Outline each Plasmodium falciparum-infected red blood cell.
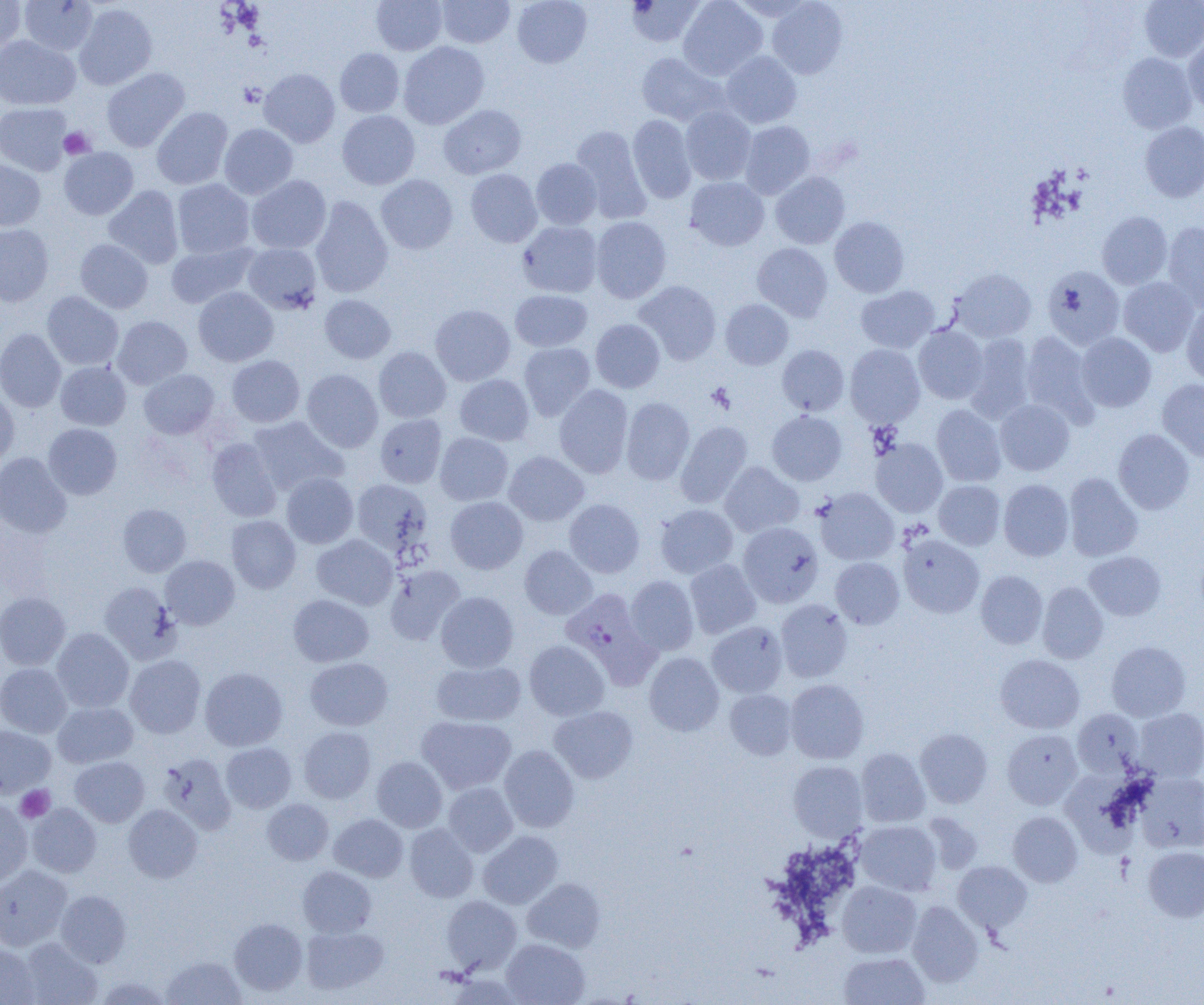

Approximate bounding boxes as named x1/y1/x2/y2 corners in pixels.
Plasmodium falciparum-infected red blood cells: (x1=560, y1=588, x2=657, y2=685).

slide_level_diagnosis: Plasmodium falciparum
field_of_view: single
uninfected_red_blood_cell_locations: 'approximate bounding boxes as named x1/y1/x2/y2 corners in pixels: (x1=0, y1=0, x2=26, y2=55), (x1=19, y1=0, x2=98, y2=56), (x1=371, y1=0, x2=447, y2=55), (x1=436, y1=0, x2=514, y2=48), (x1=512, y1=0, x2=592, y2=68), (x1=626, y1=0, x2=706, y2=47), (x1=678, y1=0, x2=768, y2=80), (x1=1139, y1=0, x2=1204, y2=62), (x1=767, y1=1, x2=848, y2=78), (x1=74, y1=4, x2=158, y2=90), (x1=0, y1=36, x2=80, y2=110), (x1=1183, y1=36, x2=1204, y2=113), (x1=398, y1=42, x2=489, y2=129), (x1=335, y1=48, x2=404, y2=117), (x1=720, y1=51, x2=801, y2=128), (x1=636, y1=52, x2=725, y2=125), (x1=1118, y1=53, x2=1197, y2=134), (x1=101, y1=68, x2=190, y2=152), (x1=259, y1=68, x2=340, y2=148), (x1=0, y1=103, x2=72, y2=175), (x1=439, y1=105, x2=525, y2=179), (x1=151, y1=107, x2=233, y2=190), (x1=680, y1=107, x2=756, y2=185), (x1=337, y1=110, x2=420, y2=189), (x1=628, y1=114, x2=697, y2=204), (x1=739, y1=121, x2=815, y2=199), (x1=1139, y1=121, x2=1204, y2=202), (x1=219, y1=123, x2=298, y2=199), (x1=570, y1=126, x2=651, y2=223), (x1=59, y1=147, x2=139, y2=219), (x1=531, y1=158, x2=602, y2=229), (x1=0, y1=159, x2=45, y2=230), (x1=465, y1=169, x2=542, y2=248), (x1=770, y1=171, x2=850, y2=249), (x1=376, y1=174, x2=457, y2=254), (x1=246, y1=175, x2=331, y2=254), (x1=685, y1=177, x2=769, y2=250), (x1=172, y1=179, x2=255, y2=259), (x1=103, y1=185, x2=184, y2=269), (x1=310, y1=196, x2=393, y2=298), (x1=1097, y1=211, x2=1172, y2=289), (x1=591, y1=216, x2=671, y2=303), (x1=830, y1=216, x2=909, y2=297), (x1=517, y1=221, x2=603, y2=297), (x1=1162, y1=222, x2=1204, y2=311), (x1=0, y1=224, x2=54, y2=306), (x1=75, y1=239, x2=153, y2=313), (x1=166, y1=241, x2=258, y2=309), (x1=243, y1=243, x2=322, y2=314), (x1=752, y1=243, x2=833, y2=321), (x1=1042, y1=266, x2=1125, y2=349), (x1=951, y1=269, x2=1036, y2=342), (x1=1118, y1=277, x2=1199, y2=356), (x1=634, y1=281, x2=721, y2=365), (x1=193, y1=286, x2=279, y2=366), (x1=855, y1=286, x2=940, y2=353), (x1=510, y1=289, x2=593, y2=352), (x1=42, y1=291, x2=124, y2=370), (x1=319, y1=294, x2=396, y2=364), (x1=720, y1=299, x2=793, y2=369), (x1=1181, y1=303, x2=1204, y2=386), (x1=430, y1=304, x2=515, y2=385), (x1=112, y1=316, x2=192, y2=389), (x1=591, y1=318, x2=665, y2=393), (x1=914, y1=325, x2=989, y2=404), (x1=0, y1=328, x2=66, y2=412), (x1=1021, y1=330, x2=1100, y2=426), (x1=1076, y1=333, x2=1156, y2=412), (x1=964, y1=334, x2=1035, y2=422), (x1=519, y1=343, x2=595, y2=421), (x1=845, y1=344, x2=925, y2=427), (x1=777, y1=345, x2=849, y2=416), (x1=374, y1=346, x2=451, y2=423), (x1=227, y1=355, x2=305, y2=427), (x1=55, y1=361, x2=131, y2=430), (x1=139, y1=369, x2=219, y2=439), (x1=302, y1=369, x2=383, y2=452), (x1=454, y1=374, x2=535, y2=445), (x1=1157, y1=379, x2=1204, y2=462), (x1=554, y1=384, x2=633, y2=478), (x1=0, y1=389, x2=19, y2=467), (x1=621, y1=397, x2=695, y2=485), (x1=995, y1=399, x2=1074, y2=475), (x1=931, y1=404, x2=1006, y2=486), (x1=767, y1=410, x2=847, y2=485), (x1=375, y1=414, x2=447, y2=488), (x1=248, y1=416, x2=349, y2=496), (x1=676, y1=421, x2=752, y2=508), (x1=43, y1=424, x2=122, y2=499), (x1=1113, y1=428, x2=1195, y2=514), (x1=435, y1=432, x2=513, y2=506), (x1=207, y1=437, x2=283, y2=522), (x1=871, y1=438, x2=948, y2=517), (x1=504, y1=451, x2=589, y2=526), (x1=0, y1=452, x2=71, y2=537), (x1=719, y1=461, x2=804, y2=537), (x1=282, y1=473, x2=358, y2=548), (x1=1064, y1=473, x2=1143, y2=562), (x1=351, y1=479, x2=433, y2=560), (x1=999, y1=479, x2=1074, y2=561), (x1=934, y1=480, x2=1005, y2=550), (x1=814, y1=488, x2=899, y2=565), (x1=445, y1=496, x2=528, y2=574), (x1=564, y1=499, x2=645, y2=578), (x1=117, y1=503, x2=191, y2=577), (x1=655, y1=503, x2=738, y2=579), (x1=226, y1=515, x2=301, y2=593), (x1=738, y1=523, x2=823, y2=607), (x1=311, y1=534, x2=397, y2=609), (x1=899, y1=535, x2=984, y2=617), (x1=520, y1=545, x2=597, y2=619), (x1=1084, y1=550, x2=1166, y2=620), (x1=160, y1=555, x2=240, y2=630), (x1=830, y1=557, x2=904, y2=629), (x1=685, y1=559, x2=761, y2=638), (x1=384, y1=565, x2=465, y2=645), (x1=975, y1=570, x2=1048, y2=648), (x1=626, y1=575, x2=699, y2=656), (x1=1038, y1=581, x2=1108, y2=664), (x1=99, y1=582, x2=180, y2=663), (x1=436, y1=591, x2=518, y2=672), (x1=0, y1=592, x2=70, y2=670), (x1=288, y1=594, x2=374, y2=667), (x1=775, y1=599, x2=853, y2=682), (x1=707, y1=621, x2=787, y2=697), (x1=52, y1=628, x2=134, y2=712), (x1=524, y1=640, x2=609, y2=720), (x1=1106, y1=640, x2=1191, y2=721), (x1=644, y1=652, x2=724, y2=736), (x1=125, y1=654, x2=206, y2=738), (x1=995, y1=654, x2=1084, y2=733), (x1=305, y1=657, x2=393, y2=731), (x1=431, y1=660, x2=526, y2=726), (x1=0, y1=663, x2=72, y2=738), (x1=200, y1=667, x2=288, y2=751), (x1=785, y1=679, x2=869, y2=764), (x1=725, y1=688, x2=797, y2=760), (x1=52, y1=701, x2=138, y2=768), (x1=549, y1=705, x2=638, y2=783), (x1=1132, y1=707, x2=1204, y2=783), (x1=1072, y1=709, x2=1144, y2=777), (x1=416, y1=716, x2=516, y2=794), (x1=0, y1=725, x2=55, y2=797), (x1=298, y1=727, x2=376, y2=803), (x1=915, y1=728, x2=993, y2=808), (x1=1002, y1=729, x2=1082, y2=809), (x1=221, y1=742, x2=296, y2=813), (x1=499, y1=744, x2=579, y2=832), (x1=856, y1=748, x2=930, y2=826), (x1=158, y1=753, x2=236, y2=834), (x1=70, y1=756, x2=149, y2=827), (x1=372, y1=756, x2=447, y2=832), (x1=788, y1=761, x2=867, y2=840), (x1=1063, y1=772, x2=1144, y2=866), (x1=1136, y1=773, x2=1204, y2=852), (x1=443, y1=782, x2=518, y2=856), (x1=0, y1=799, x2=33, y2=886), (x1=262, y1=799, x2=334, y2=865), (x1=27, y1=803, x2=101, y2=877), (x1=123, y1=804, x2=203, y2=882), (x1=1008, y1=811, x2=1082, y2=887), (x1=329, y1=813, x2=408, y2=882), (x1=922, y1=813, x2=983, y2=874), (x1=856, y1=820, x2=941, y2=895), (x1=405, y1=824, x2=478, y2=902), (x1=478, y1=830, x2=563, y2=909), (x1=1143, y1=846, x2=1204, y2=922), (x1=953, y1=861, x2=1032, y2=932), (x1=0, y1=865, x2=72, y2=951), (x1=298, y1=865, x2=376, y2=937), (x1=523, y1=878, x2=605, y2=952), (x1=837, y1=881, x2=921, y2=958), (x1=56, y1=890, x2=130, y2=967), (x1=441, y1=895, x2=521, y2=974), (x1=907, y1=901, x2=984, y2=987), (x1=229, y1=918, x2=308, y2=995), (x1=301, y1=925, x2=388, y2=995), (x1=19, y1=937, x2=103, y2=1005), (x1=501, y1=938, x2=590, y2=1005), (x1=0, y1=944, x2=40, y2=1004), (x1=839, y1=952, x2=930, y2=1005), (x1=161, y1=955, x2=246, y2=1004), (x1=94, y1=976, x2=174, y2=1004)'
preparation: thin blood smear
modality: optical microscopy
magnification: 1000x
image_size: 1204×1005 pixels
platelet_locations: 'approximate bounding boxes as named x1/y1/x2/y2 corners in pixels: (x1=59, y1=127, x2=95, y2=158), (x1=706, y1=383, x2=735, y2=413), (x1=16, y1=785, x2=55, y2=823)'